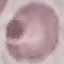

Result: negative for malaria parasites. Giemsa-stained preparation. Cell patch, automatically extracted from a larger field of view and resized to 64 × 64 pixels. Photographed with a smartphone camera at the microscope eyepiece. Thin smear of blood.